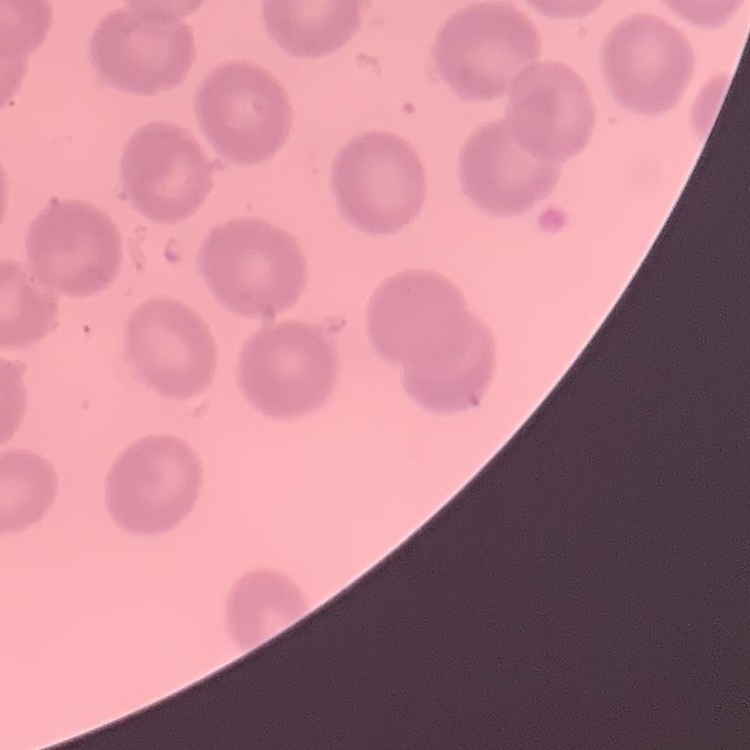

red blood cell morphology = no rouleaux formation
preparation = thin peripheral smear
stain = Field's or Giemsa
image type = one tile cut from a larger photomicrograph